State which parasite is depicted.
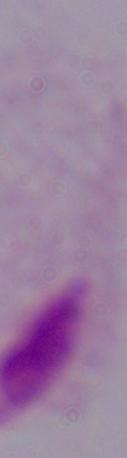
A trichomonad.

Summary:
  - Modality: photomicrograph
  - Magnification: 1000x